Name the cell type shown.
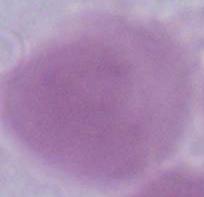
This is an erythrocyte.

Summary:
  - Modality: photomicrograph
  - Magnification: 1000x